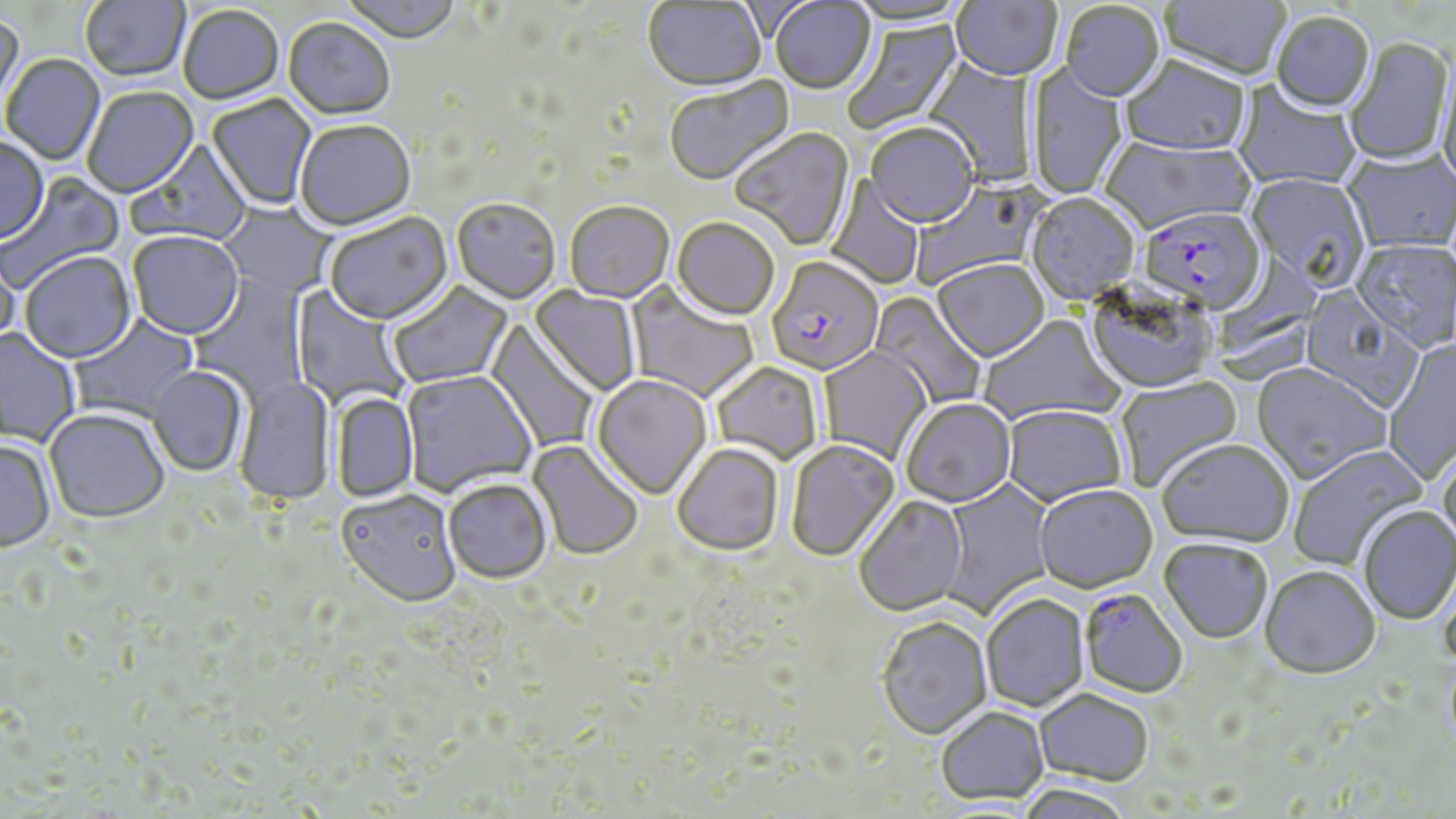
Approximate bounding boxes as (x1,y1)-(x2,y2) corner pairs in pixels. Plasmodium falciparum-infected red blood cell locations: (1144,212)-(1271,317), (767,257)-(884,378), (1079,589)-(1188,699). Uninfected red blood cell locations: (80,0)-(190,84), (339,0)-(462,46), (771,0)-(876,96), (844,0)-(971,28), (951,0)-(1061,83), (1160,0)-(1290,84), (643,1)-(767,94), (1060,3)-(1165,104), (178,7)-(284,106), (0,13)-(27,120), (1271,13)-(1375,115), (843,17)-(965,135), (283,20)-(394,122), (1345,38)-(1453,168), (1436,50)-(1456,193), (924,54)-(1037,187), (2,55)-(105,167), (1119,58)-(1250,159), (1026,61)-(1129,202), (664,76)-(796,189), (1233,82)-(1362,191), (83,88)-(199,199), (206,94)-(316,212), (296,122)-(416,233), (866,125)-(978,231), (731,128)-(856,252), (1099,136)-(1254,237), (0,138)-(49,246), (128,140)-(252,248), (1342,149)-(1456,256), (0,171)-(126,295), (1244,174)-(1370,290), (825,175)-(925,290), (910,178)-(1047,289), (1027,194)-(1140,306), (452,201)-(560,306), (219,203)-(334,297), (565,204)-(675,305), (325,213)-(453,327), (671,219)-(779,323), (128,233)-(244,342), (1351,240)-(1456,353), (0,248)-(22,359), (19,254)-(136,365), (933,261)-(1049,364), (188,273)-(311,400), (387,281)-(514,389), (624,282)-(759,403), (290,285)-(411,409), (1086,285)-(1217,395), (529,286)-(640,397), (1300,287)-(1423,412), (869,291)-(986,409), (69,312)-(200,424), (979,315)-(1124,426), (484,320)-(600,452), (0,328)-(80,448), (1382,339)-(1456,484), (819,347)-(932,463), (1251,363)-(1391,484), (711,364)-(823,465), (147,367)-(247,477), (401,371)-(538,498), (1115,374)-(1244,492), (233,375)-(335,507), (592,375)-(712,501), (331,393)-(418,502), (901,400)-(1017,510), (1002,407)-(1127,509), (44,409)-(170,525), (0,440)-(56,553), (527,440)-(643,562), (787,441)-(901,563), (1157,441)-(1294,549), (1437,441)-(1456,554), (1287,444)-(1429,572), (673,446)-(785,558), (938,477)-(1056,618), (444,482)-(552,585), (1034,487)-(1158,595), (336,492)-(462,611), (854,496)-(968,618), (1358,506)-(1456,626), (1159,540)-(1273,645), (1260,567)-(1380,681), (981,595)-(1090,713), (877,618)-(992,741), (1035,688)-(1155,786), (934,707)-(1049,804), (1014,784)-(1138,818). Slide-level diagnosis: Plasmodium falciparum. 1000x magnification. Image is 1456×819 pixels. Single field of view. Optical microscopy. May-Grünwald-Giemsa-stained preparation. Thin blood smear.